Report the malaria status of this cell.
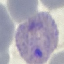
It is parasitized.

Summary:
  - Capture: smartphone through the microscope eyepiece
  - Stain: Giemsa
  - Image type: cell patch, automatically extracted from a larger field of view and resized to 64 × 64 pixels
  - Preparation: thin blood smear